Name the cell type shown.
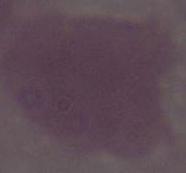

An erythrocyte.

1000x magnification. Photomicrograph.